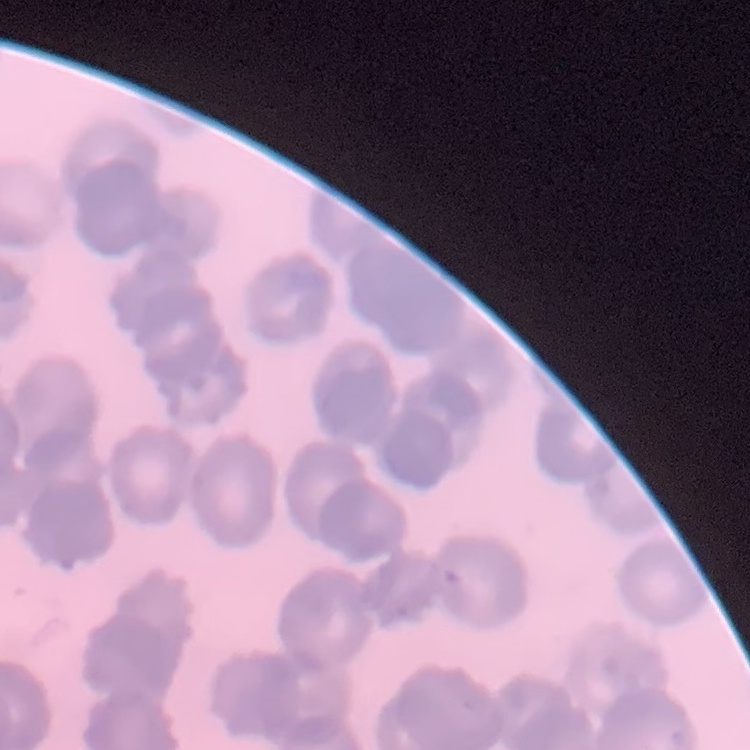
The red blood cells exhibit rouleaux formation. Stained with either Field's or Giemsa. Thin blood film. Square crop of a larger photomicrograph.